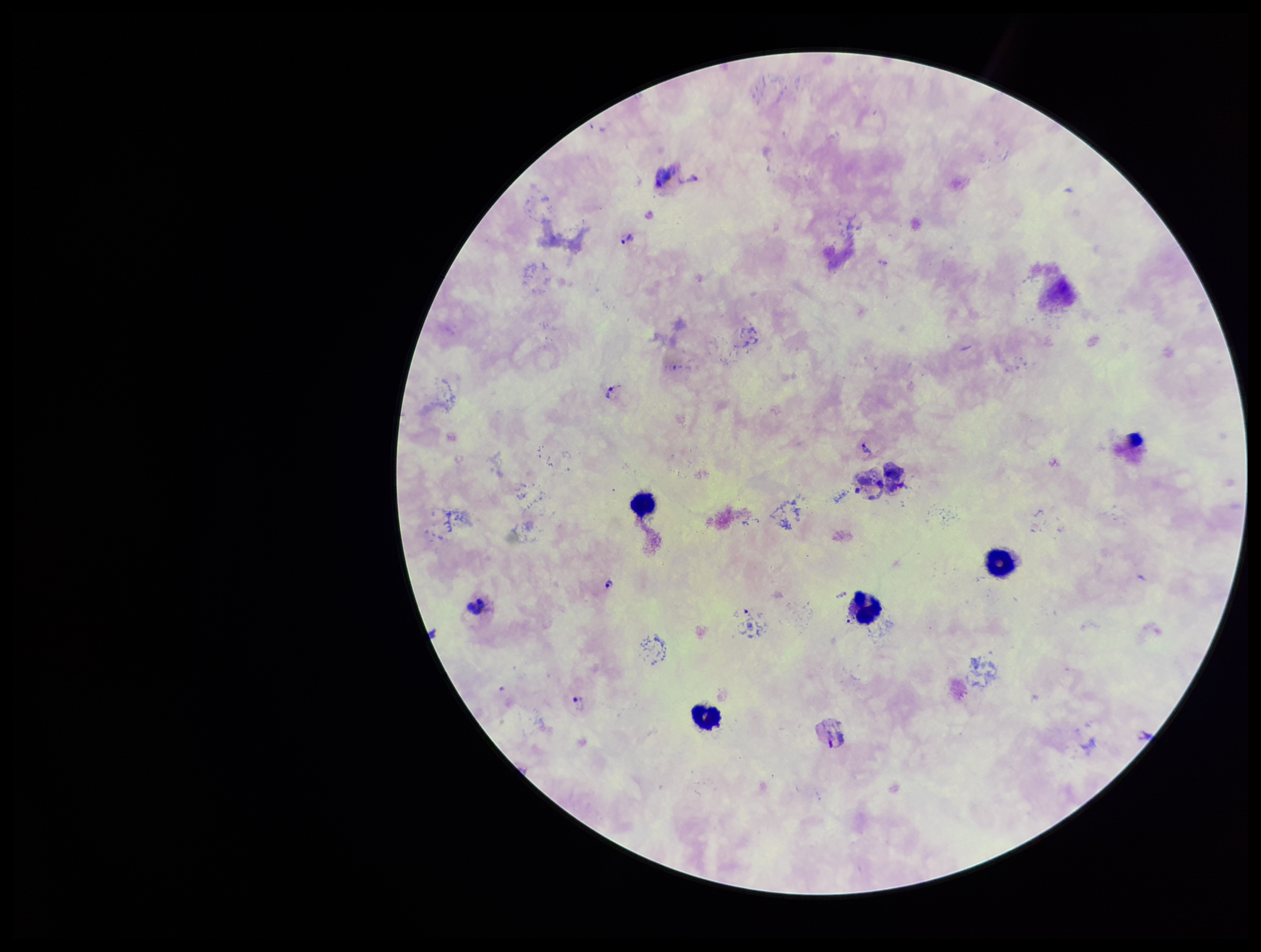

Summary:
  - Patient malaria status: infected
  - Species reported for this patient: Plasmodium vivax
  - Field of view: one from this slide
  - Plasmodium parasites: detected
  - Leukocyte count: 7
  - Capture: smartphone photograph through the microscope eyepiece
  - Image size: 1261×952 pixels
  - Stain: Giemsa
  - Preparation: thick smear
  - Parasite count: 10